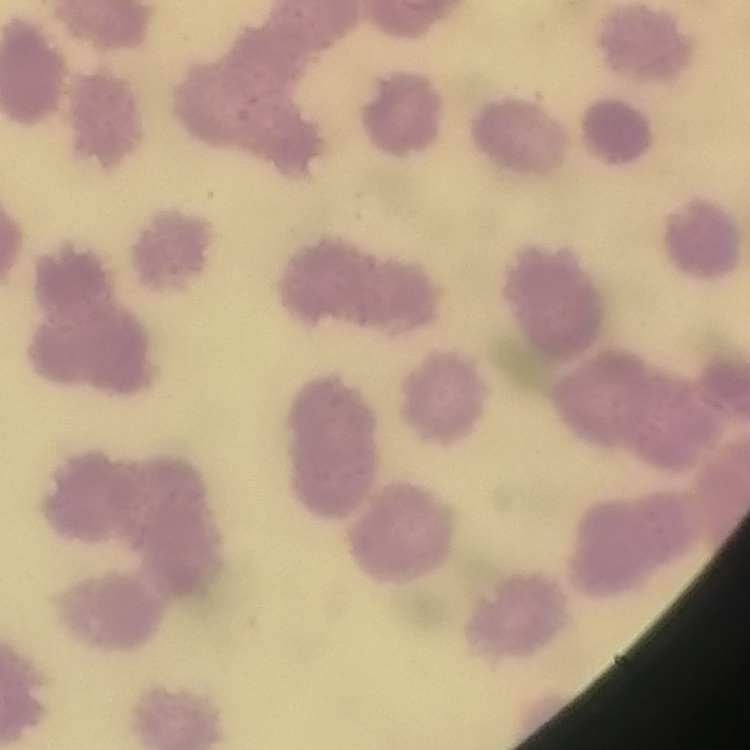

Summary:
  - Red blood cell morphology: rouleaux formation
  - Stain: Field's or Giemsa
  - Preparation: thin blood smear
  - Image type: square crop of a larger photomicrograph